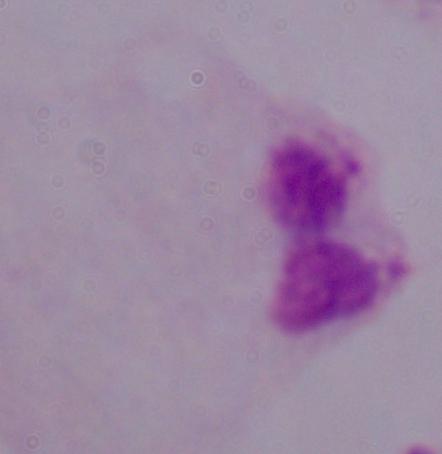 A trichomonad is shown. Photomicrograph. 1000x magnification.